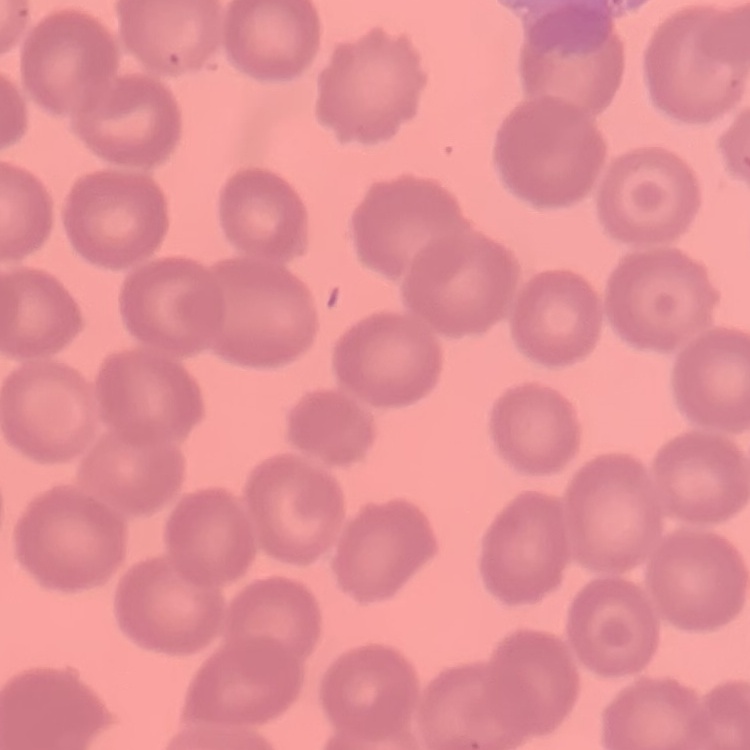
erythrocyte morphology = no rouleaux formation
preparation = thin peripheral smear
image type = one tile cut from a larger photomicrograph
stain = Field's or Giemsa